Locate the cells, classifying each as a parasitized red blood cell, an uninfected red blood cell, or a white blood cell.
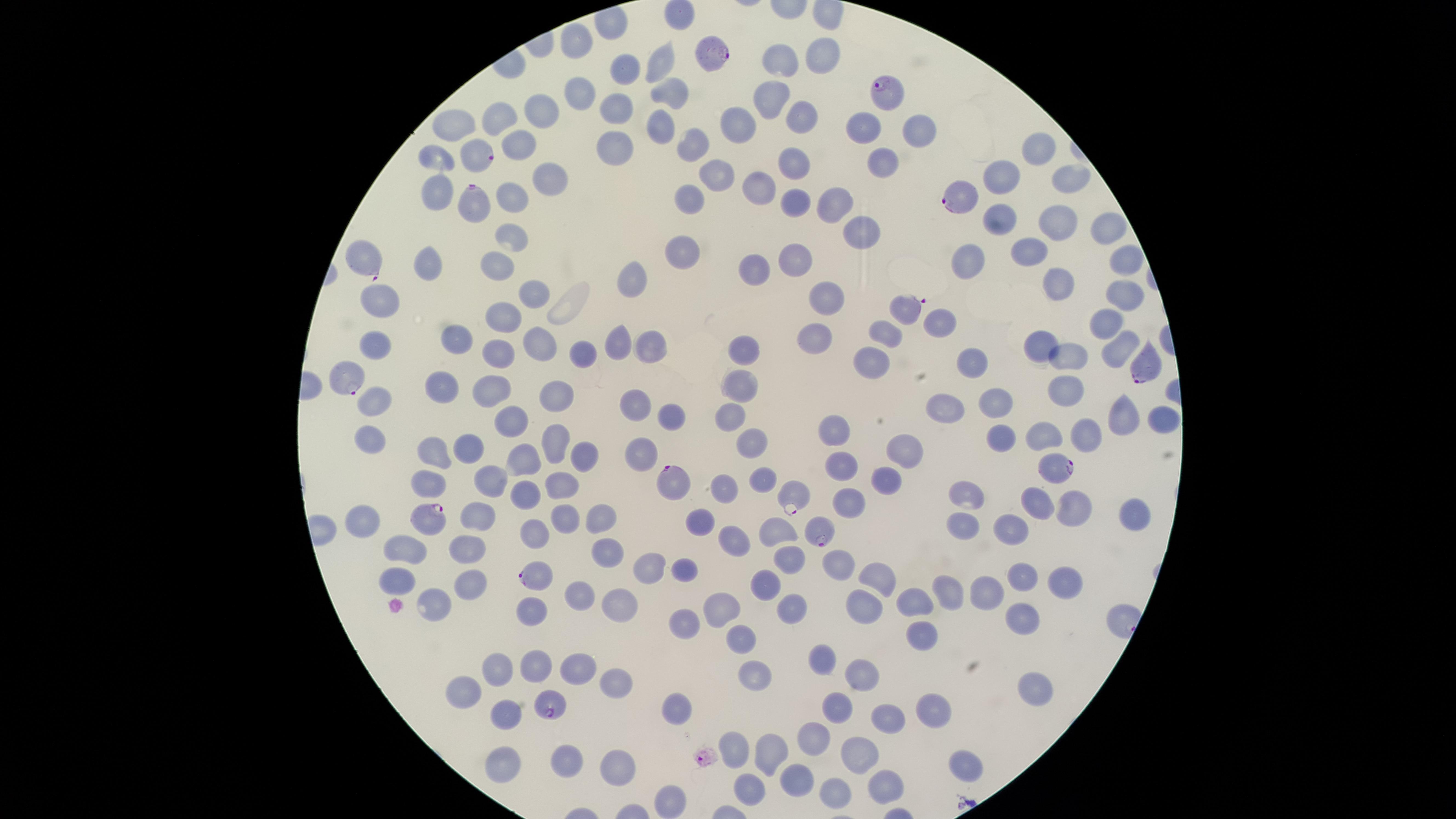
Approximate marker points as [x, y] in pixels.
Parasitized red blood cells: [714, 53], [888, 95], [480, 156], [955, 198], [472, 200], [358, 260], [905, 310], [1149, 367], [344, 377], [1053, 465], [668, 479], [790, 495], [423, 518], [817, 530], [537, 577], [553, 707].
Uninfected red blood cells: [677, 14], [576, 44], [820, 57], [660, 62], [777, 66], [619, 75], [672, 88], [580, 89], [770, 99], [618, 105], [541, 107], [497, 119], [802, 119], [740, 124], [658, 126], [456, 127], [864, 130], [919, 131], [521, 140], [1041, 145], [617, 146], [686, 147], [436, 157], [794, 164], [883, 164], [1003, 175], [713, 176], [1068, 178], [547, 181], [762, 182], [434, 191], [510, 196], [687, 196], [798, 196], [841, 201], [1003, 217], [1063, 217], [1104, 227], [863, 230], [515, 238], [682, 249], [1034, 250], [429, 259], [972, 259], [1124, 259], [749, 262], [794, 263], [502, 268], [634, 280], [1065, 288], [830, 290], [1126, 290], [534, 297], [384, 301], [504, 312], [940, 319], [1111, 319], [886, 330], [372, 336], [815, 337], [453, 339], [617, 340], [1039, 344], [534, 345], [650, 345], [498, 346], [743, 346], [1117, 349], [585, 355], [1073, 358], [872, 359], [978, 364], [746, 383], [439, 386], [494, 387], [1066, 387], [555, 391], [375, 403], [995, 405], [946, 407], [629, 408], [734, 412], [1119, 413], [511, 418], [668, 418], [1158, 418], [833, 433], [1086, 435], [1002, 436], [374, 437], [1042, 437], [756, 439], [550, 443], [903, 447], [465, 450], [587, 454], [642, 454], [433, 456], [524, 458], [838, 464], [888, 477], [758, 481], [428, 482], [488, 482], [558, 483], [723, 485], [523, 491], [976, 496], [845, 499], [1037, 503], [1071, 510], [605, 515], [1130, 517], [700, 518], [477, 519], [561, 519], [963, 519], [364, 524], [772, 531], [530, 534], [1014, 534], [734, 542], [605, 544], [464, 548], [410, 554], [780, 558], [839, 562], [644, 568], [686, 571], [877, 576], [1023, 577], [396, 580], [1062, 581], [469, 584], [760, 585], [947, 588], [984, 588], [579, 598], [919, 599], [435, 602], [615, 604], [863, 604], [720, 606], [797, 608], [526, 609], [683, 616], [1024, 620], [919, 638], [739, 640], [824, 661], [531, 662], [572, 664], [497, 670], [746, 674], [864, 676], [607, 684], [1023, 689], [463, 691], [834, 707], [675, 710], [931, 710], [885, 715], [503, 719], [816, 735], [736, 746], [767, 750], [857, 751], [562, 756], [495, 765], [959, 765], [619, 766], [791, 777], [884, 783], [747, 786], [828, 790], [671, 793].
No white blood cells identified.

{
  "visible_region": "circular",
  "preparation": "thin blood smear",
  "image_size": "1456×819 pixels",
  "species": "Plasmodium falciparum",
  "capture": "smartphone photograph through the microscope eyepiece",
  "stain": "Giemsa",
  "field_of_view": "single"
}